Report the malaria status of this cell.
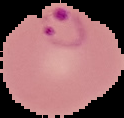

Parasitized.

Summary:
  - Image type: cell region segmented out of the field of view; surrounding area masked to black
  - Preparation: thin blood smear
  - Image size: 124×118 pixels